Name the cell type shown.
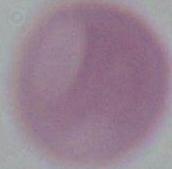

An erythrocyte.

Summary:
  - Modality: micrograph
  - Magnification: 1000x